State the blood parasite species.
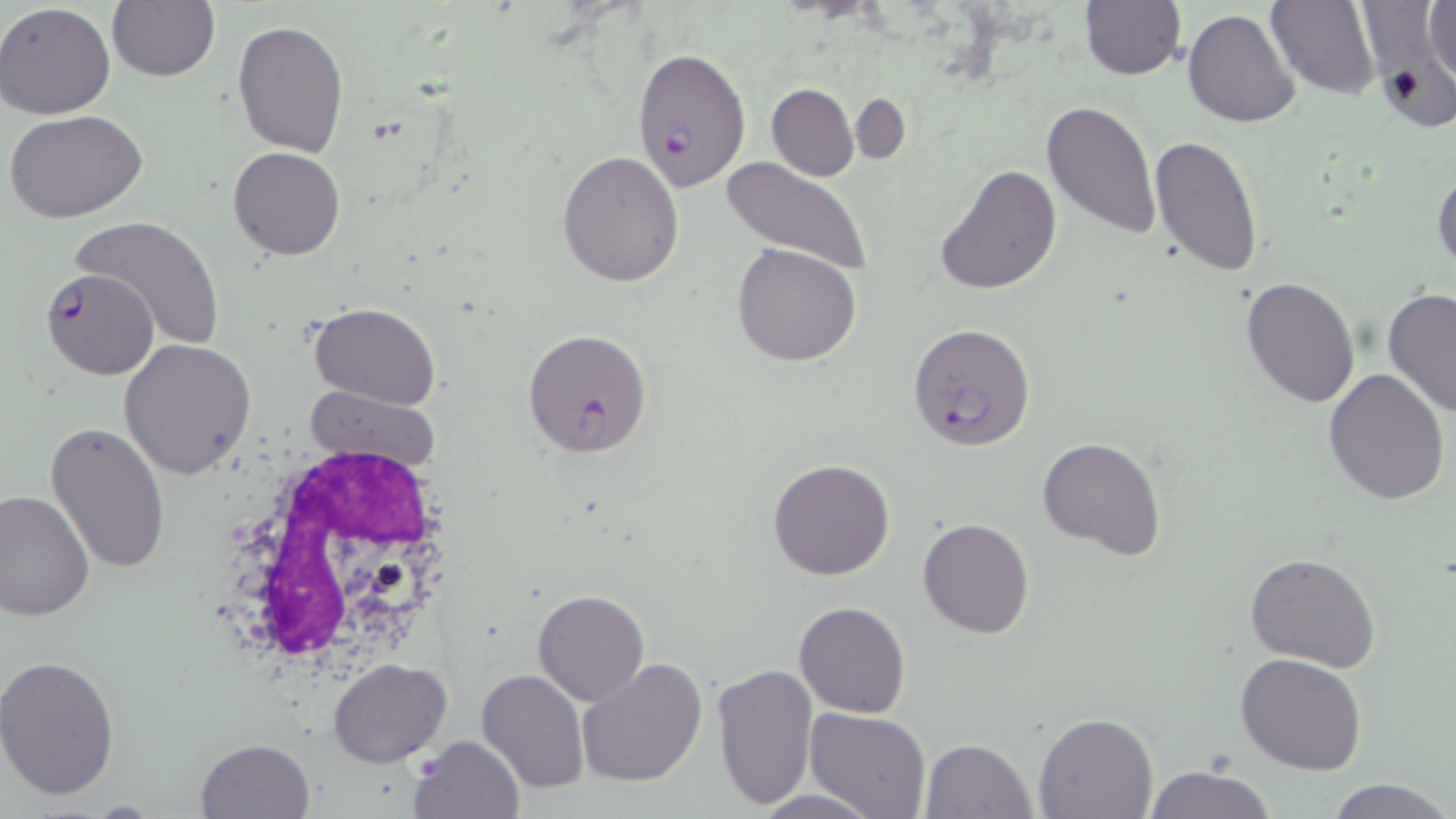

Plasmodium falciparum.

Summary:
  - Coordinate format: approximate bounding boxes as (x1,y1)-(x2,y2) corner pairs in pixels
  - Uninfected red blood cell locations: (1267,0)-(1380,99), (1079,1)-(1186,79), (1425,1)-(1455,88), (0,2)-(116,119), (106,2)-(221,82), (1184,7)-(1300,128), (233,19)-(348,158), (766,83)-(858,181), (850,94)-(910,166), (1041,98)-(1162,240), (6,110)-(149,223), (1150,135)-(1264,277), (228,146)-(345,260), (557,150)-(685,288), (720,157)-(873,278), (1432,163)-(1456,274), (937,164)-(1061,295), (68,214)-(228,351), (732,242)-(862,368), (1241,278)-(1361,407), (1382,287)-(1456,419), (308,301)-(440,408), (120,337)-(257,479), (1324,367)-(1451,505), (45,419)-(172,576), (1038,435)-(1166,559), (767,459)-(895,580), (0,488)-(94,622), (918,517)-(1035,639), (1245,552)-(1380,672), (532,589)-(650,705), (795,601)-(911,718), (1235,652)-(1367,775), (0,653)-(122,801), (328,658)-(452,765), (578,658)-(708,789), (712,662)-(819,810), (476,667)-(591,795), (803,707)-(931,818), (1033,712)-(1159,819), (410,735)-(524,818), (195,738)-(317,819), (920,739)-(1037,819), (1143,763)-(1276,819), (1326,778)-(1450,819), (746,789)-(884,817)
  - White blood cell locations: (210,444)-(459,677)
  - Plasmodium falciparum-infected red blood cell locations: (631,47)-(753,190), (41,266)-(159,379), (907,323)-(1035,450), (521,328)-(654,458)
  - Stain: May-Grünwald-Giemsa
  - Preparation: thin blood film
  - Magnification: 1000x
  - Modality: optical microscopy
  - Image size: 1456×819 pixels
  - Field of view: one of a larger specimen